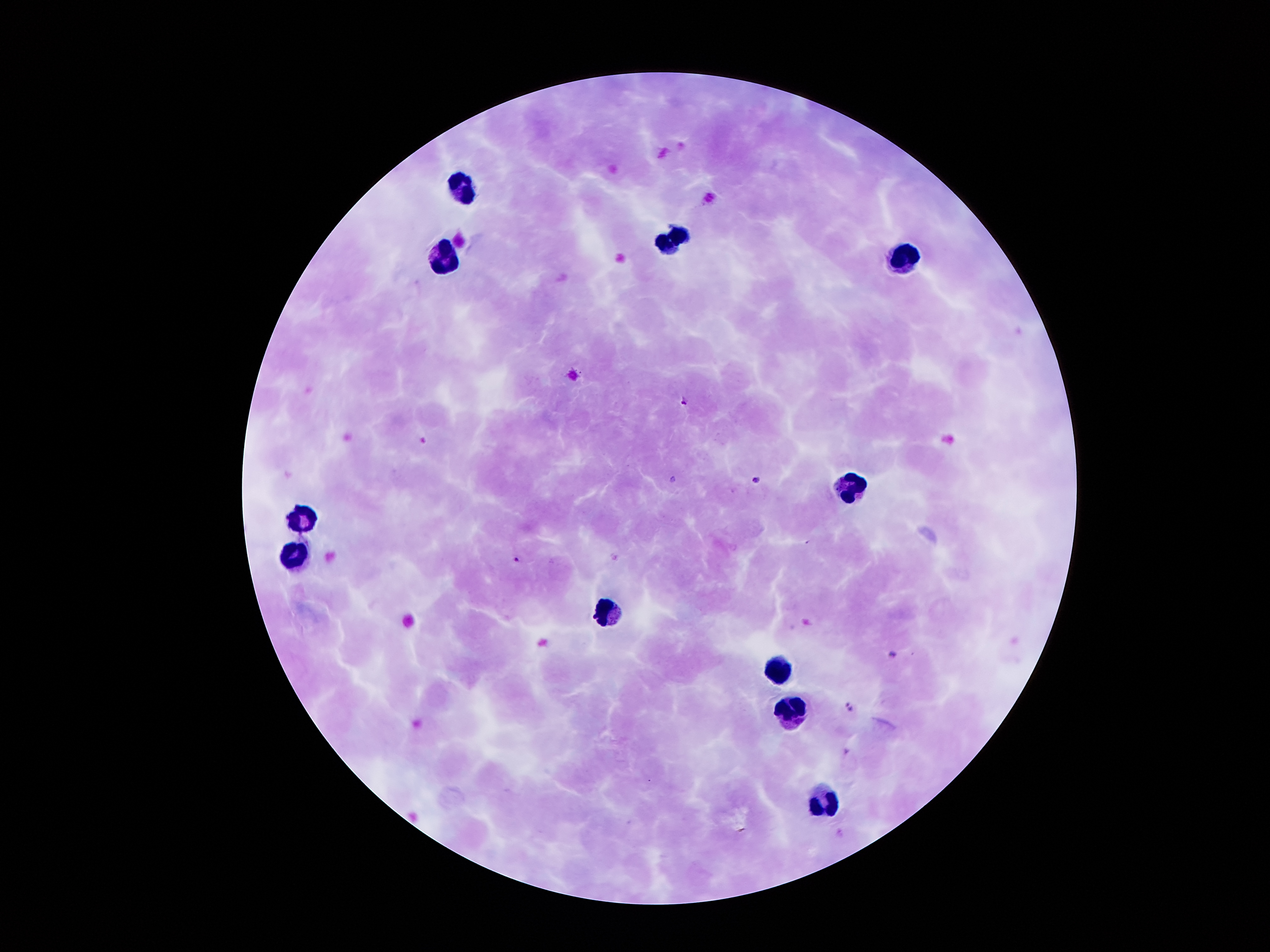 Approximate centers as {x, y} in pixels. Plasmodium parasite locations: {685, 400}, {757, 480}, {516, 559}, {892, 654}, {849, 706}. Leukocyte locations: {469, 189}, {671, 241}, {905, 255}, {440, 260}, {847, 485}, {306, 520}, {300, 551}, {605, 614}, {780, 669}, {790, 709}, {826, 802}. Image is 1270×952 pixels. Thick blood film. Giemsa-stained preparation. Patient malaria status: infected with Plasmodium falciparum. One field from this slide. Smartphone photograph taken through the microscope eyepiece. 100x magnification.